Report the malaria status of this cell.
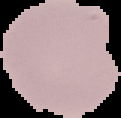

It is uninfected.

Image is 121×118 pixels. From a thin blood smear. Segmented cell region on a black background.